Comment on the morphology of the erythrocytes.
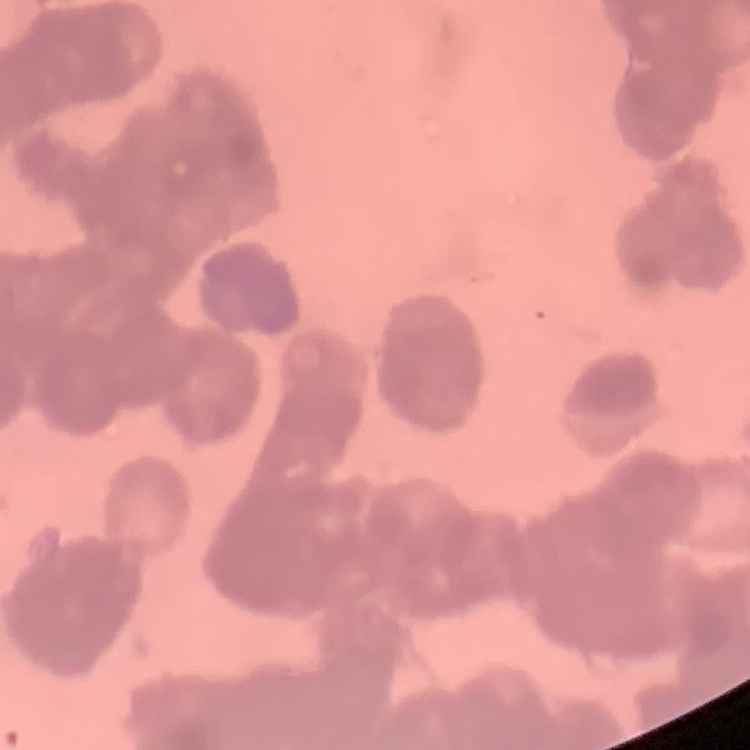
Rouleaux formation.

Thin peripheral smear. One tile cut from a larger photomicrograph. Stained with either Field's or Giemsa.